Report the malaria status of this cell.
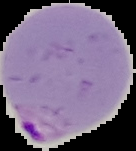

It is parasitized.

Segmented cell region on a black background. From a thin blood film. Image is 136×151 pixels.